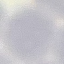

Summary:
  - Result: negative for malaria parasites
  - Preparation: thin smear
  - Image type: cell patch, automatically extracted from a larger field of view and resized to 64 × 64 pixels
  - Stain: Giemsa
  - Capture: smartphone through the microscope eyepiece